Point out each Plasmodium parasite.
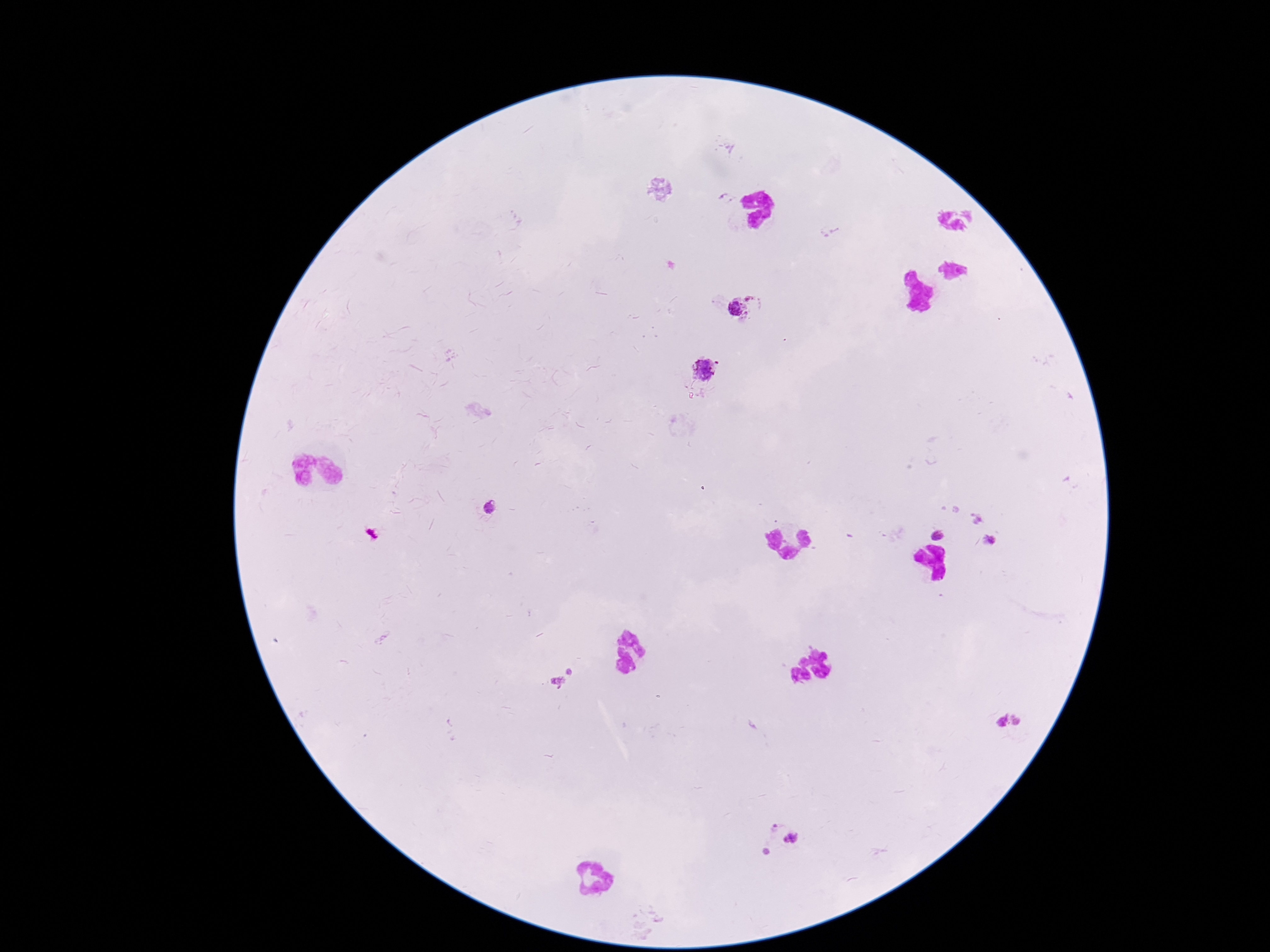
Approximate object centers, in pixels from the top-left corner.
Plasmodium parasites: (x=743, y=307), (x=707, y=370), (x=489, y=511), (x=975, y=518), (x=938, y=533), (x=989, y=542), (x=564, y=679), (x=1021, y=721), (x=1000, y=722), (x=782, y=841).

stain = Giemsa
magnification = 100x
field of view = one from this slide
image size = 1270×952 pixels
preparation = thick blood film
patient malaria status = positive
capture = smartphone camera through the microscope eyepiece